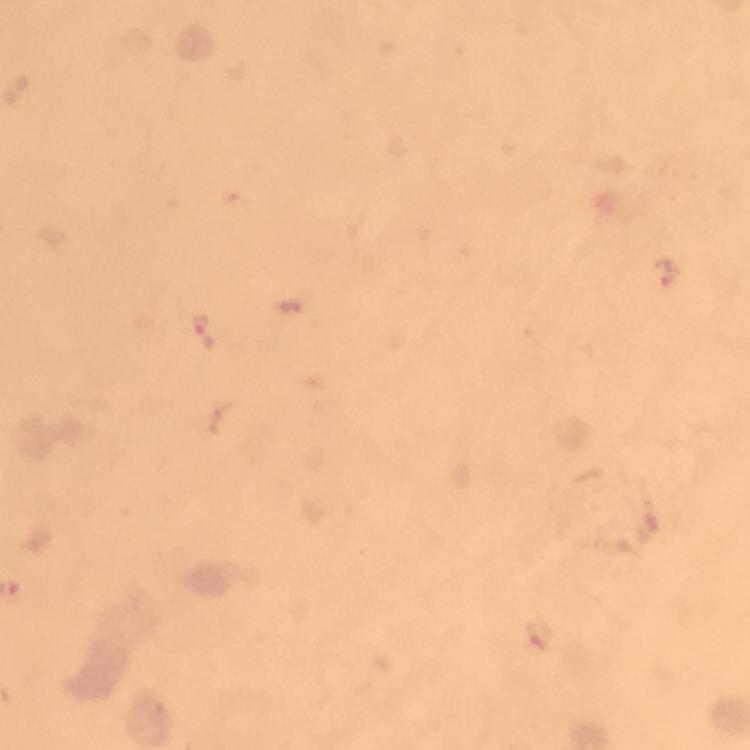

{
  "immersion_oil": "used",
  "malaria_parasite_locations": "approximate centers as {x, y} in pixels: {665, 273}, {285, 305}, {203, 330}, {537, 634}",
  "image_size": "750×750 pixels",
  "magnification": "100x",
  "preparation": "thick smear",
  "context": "from a diagnostic examination for malaria",
  "cropped_from": "a single field of view",
  "capture": "smartphone mounted on the microscope",
  "stain": "Giemsa"
}